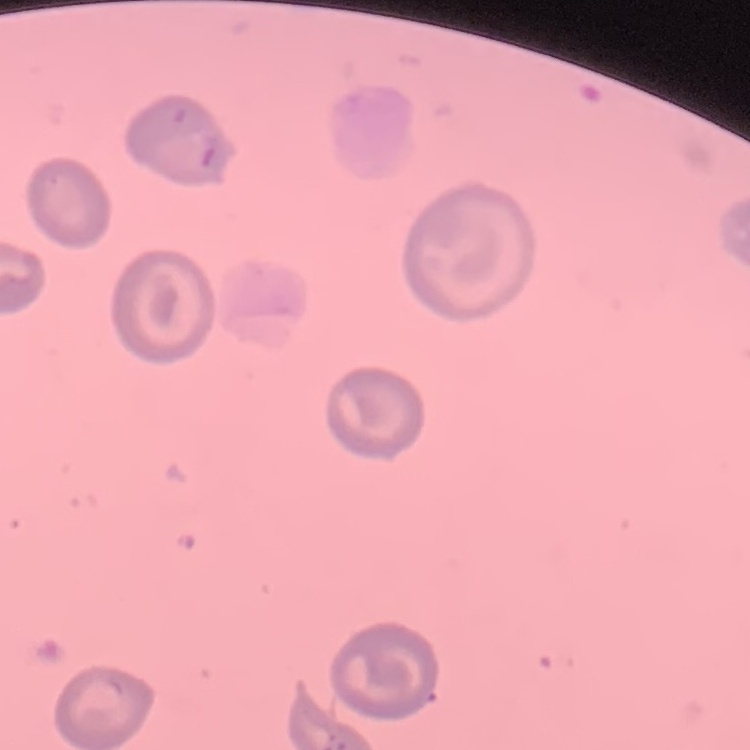

{
  "red_blood_cell_morphology": "no rouleaux formation",
  "image_type": "one tile cut from a larger photomicrograph",
  "preparation": "thin peripheral smear",
  "stain": "Field's or Giemsa"
}